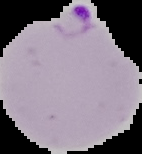

result = Plasmodium parasites identified
image size = 142×154 pixels
image type = cell region segmented out of the field of view; surrounding area masked to black
preparation = thin blood smear